Locate the red blood cells and classify each one as P. falciparum-infected, uninfected, or of indeterminate infection status.
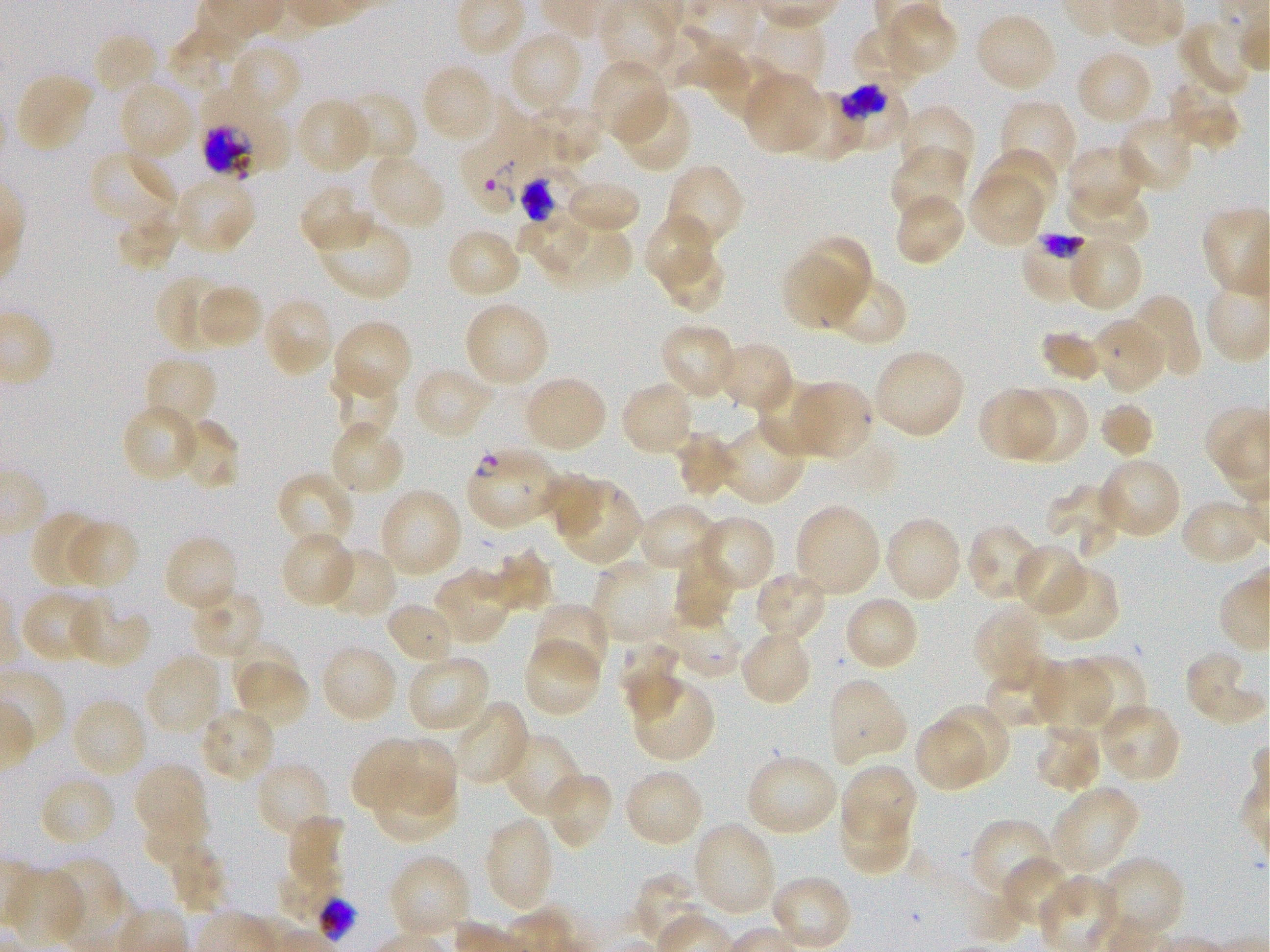
Approximate bounding boxes as (x1, y1, x2, y2) in pixels. Not every red blood cell is marked. A life-cycle stage — or a range of stages, where the recorded stages span more than one — follows each staged infected red blood cell.
Infected red blood cells: (833, 83, 911, 153) trophozoite; (198, 85, 287, 179); (462, 95, 550, 215) late ring to early trophozoite; (1021, 231, 1094, 305) trophozoite; (466, 447, 562, 529) ring.
Red blood cells of indeterminate infection status: (521, 160, 582, 223), (277, 859, 342, 923).
Uninfected red blood cells: (883, 4, 957, 76), (975, 12, 1058, 92), (750, 14, 827, 92), (1178, 19, 1253, 99), (669, 24, 745, 92), (850, 24, 925, 90), (165, 26, 247, 93), (507, 29, 585, 114), (92, 32, 160, 100), (229, 43, 303, 119), (1075, 49, 1152, 126), (712, 52, 784, 123), (591, 58, 669, 144), (420, 63, 497, 144), (14, 72, 95, 153), (744, 73, 825, 153), (118, 80, 196, 163), (1165, 80, 1242, 149), (786, 90, 859, 162), (341, 92, 417, 166), (615, 92, 693, 173), (294, 97, 372, 175), (998, 99, 1076, 184), (529, 102, 606, 167), (895, 105, 977, 183), (1116, 114, 1195, 193), (1065, 145, 1147, 217), (890, 146, 968, 223), (986, 146, 1058, 219), (89, 148, 177, 227), (367, 152, 447, 232), (664, 163, 747, 250), (968, 171, 1047, 248), (174, 173, 257, 254), (565, 180, 639, 234), (298, 184, 370, 254), (1066, 187, 1150, 245), (893, 193, 965, 267), (117, 209, 182, 272), (516, 213, 592, 275), (644, 213, 714, 288), (316, 216, 413, 301), (445, 227, 522, 299), (543, 228, 634, 294), (1067, 234, 1145, 312), (788, 243, 869, 327), (658, 248, 727, 314), (806, 258, 890, 335), (825, 273, 909, 347), (154, 276, 229, 353), (197, 284, 263, 350), (1125, 294, 1202, 379), (263, 296, 335, 378), (462, 301, 551, 387), (1092, 316, 1166, 395), (331, 319, 413, 400), (659, 324, 737, 401), (1042, 331, 1101, 381), (714, 341, 795, 413), (872, 348, 965, 440), (142, 355, 219, 430), (412, 366, 495, 441), (329, 370, 398, 442), (523, 375, 608, 453), (757, 378, 831, 458), (620, 380, 695, 458), (794, 381, 873, 460), (1010, 385, 1089, 465), (977, 387, 1054, 462), (1098, 400, 1155, 460), (120, 402, 201, 484), (176, 419, 240, 492), (329, 421, 405, 497), (719, 421, 805, 506), (676, 431, 740, 499), (1098, 456, 1182, 539), (276, 470, 356, 549), (542, 473, 606, 535), (555, 479, 643, 565), (1046, 483, 1126, 561), (378, 488, 464, 578), (1179, 497, 1262, 567), (636, 502, 720, 574), (794, 504, 882, 596), (30, 511, 105, 590), (695, 515, 776, 594), (883, 516, 963, 603), (63, 518, 138, 590), (965, 522, 1046, 603), (279, 532, 355, 608), (163, 535, 238, 614), (1013, 544, 1088, 618), (322, 547, 398, 621), (490, 550, 555, 615), (671, 550, 735, 629), (591, 561, 673, 645), (1038, 564, 1121, 643), (433, 568, 511, 645), (753, 569, 828, 643), (190, 588, 266, 658), (20, 589, 105, 664), (844, 595, 921, 673), (68, 598, 152, 668), (384, 600, 456, 666), (532, 601, 611, 680), (972, 601, 1050, 689), (659, 607, 744, 679), (738, 629, 813, 707), (615, 637, 684, 722), (522, 638, 602, 718), (232, 643, 303, 704), (320, 644, 398, 724), (1184, 651, 1266, 724), (144, 652, 222, 734), (1072, 653, 1148, 732), (406, 654, 492, 734), (234, 656, 309, 729), (982, 658, 1070, 728), (1034, 659, 1109, 732), (630, 676, 715, 763), (827, 676, 908, 768), (71, 697, 149, 778), (453, 699, 533, 787), (1098, 702, 1182, 784), (933, 705, 1008, 783), (197, 707, 277, 784), (913, 715, 988, 792), (1032, 722, 1103, 792), (501, 733, 583, 817), (352, 737, 432, 812), (389, 739, 459, 816), (744, 752, 839, 837), (255, 761, 333, 840), (133, 762, 209, 846), (841, 763, 917, 846), (623, 768, 705, 849), (541, 771, 614, 849), (372, 773, 457, 844), (37, 774, 116, 848), (1050, 785, 1141, 875), (839, 800, 912, 878), (143, 804, 210, 863), (287, 814, 345, 886), (484, 816, 556, 912), (970, 817, 1054, 899), (692, 821, 778, 917), (169, 842, 229, 914), (387, 855, 472, 939), (47, 857, 127, 944), (1001, 857, 1077, 932), (1099, 857, 1186, 944), (8, 868, 85, 945), (632, 873, 711, 948), (770, 875, 853, 951).

Image is 1270×952 pixels. Life-cycle stages observed: ring, trophozoite. Thin blood smear. 100x objective under oil immersion, numerical aperture 1.25. Static in-vitro culture of P. falciparum strain 3D7. Giemsa-stained preparation. Donor blood group O+. One field from this slide.